Assess the morphology of the erythrocytes.
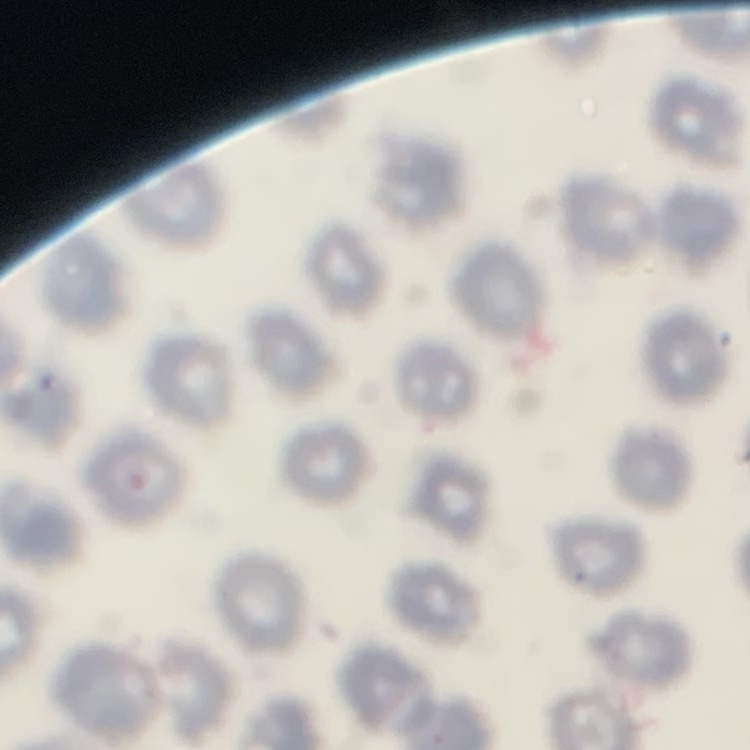
They show no rouleaux formation.

image_type: square crop of a larger photomicrograph
stain: Field's or Giemsa
preparation: thin blood smear